Assess this cell for malaria.
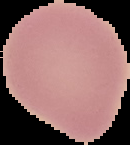
It is uninfected.

From a thin blood film. Cell region segmented out of the field of view; the surrounding area is masked to black. Image is 130×145 pixels.